Comment on the morphology of the red blood cells.
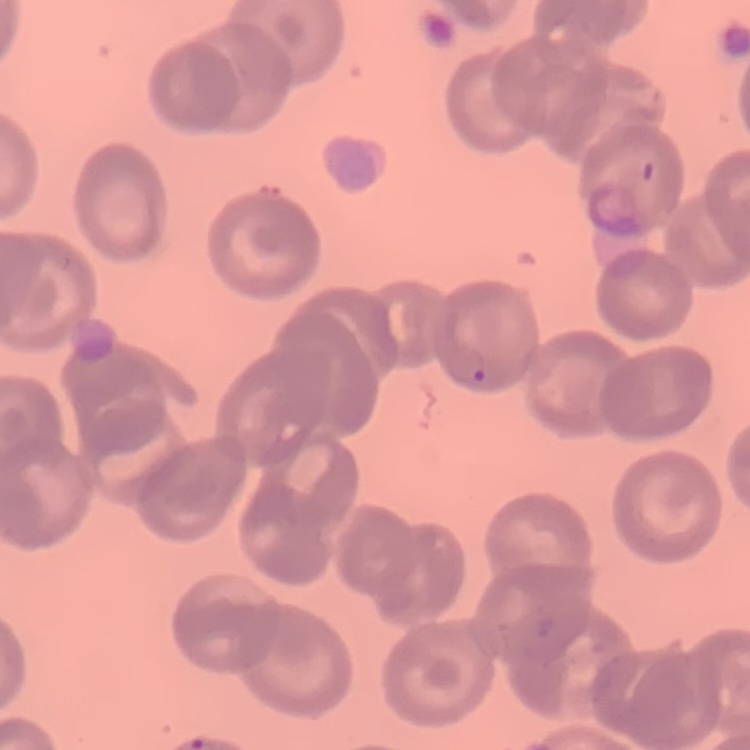

No rouleaux formation.

Thin peripheral smear. One tile cut from a larger photomicrograph. Stained with either Field's or Giemsa.